Report the malaria status of this cell.
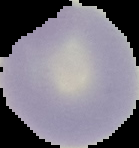

Uninfected.

Summary:
  - Image size: 139×148 pixels
  - Image type: segmented cell region on a black background
  - Preparation: thin blood film